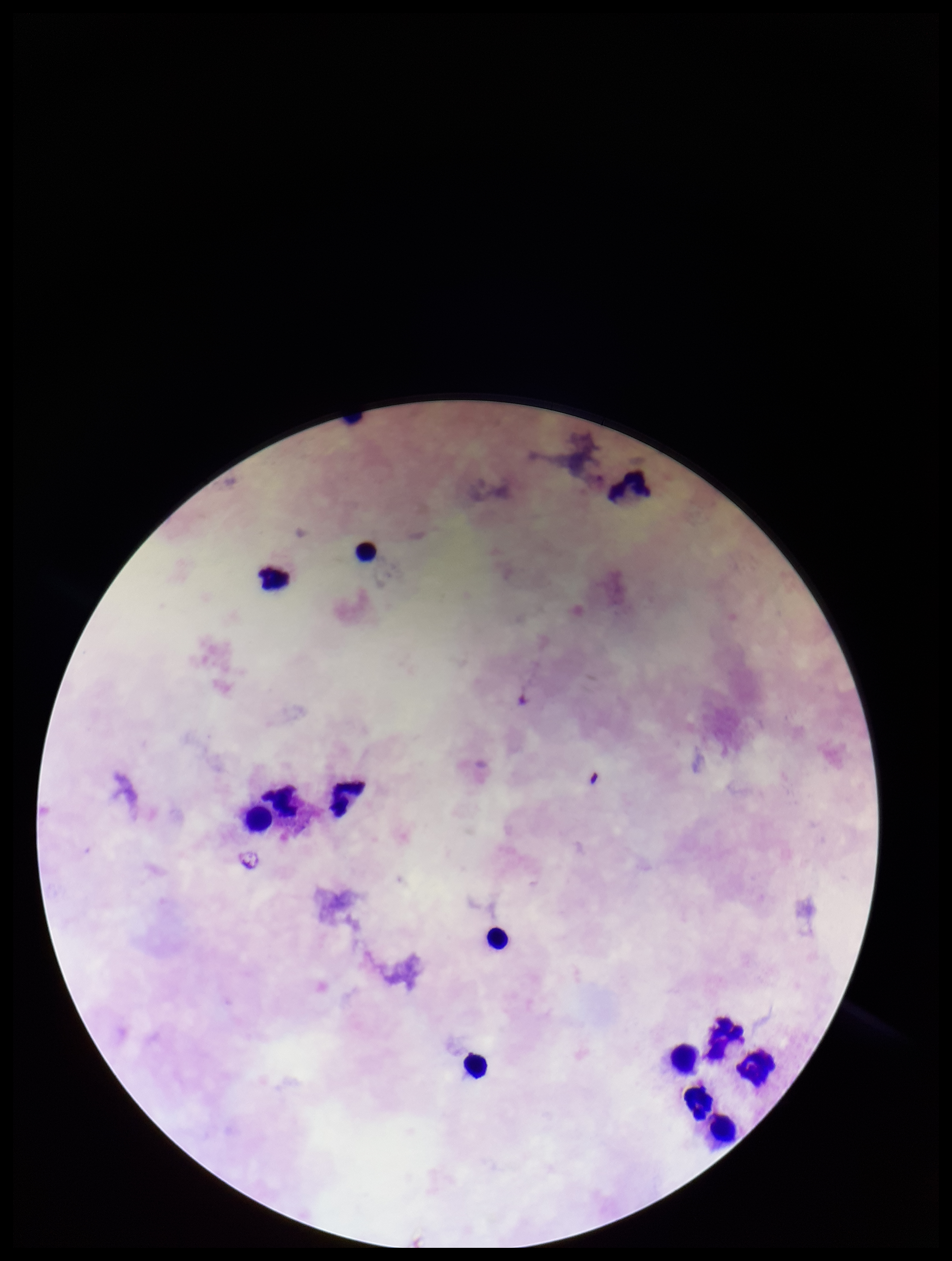 Photographed through the microscope eyepiece with a smartphone camera. Plasmodium parasites: none seen. Preparation: thick smear. Image is 952×1261 pixels. Leukocyte count: 13. Patient malaria status: negative. Parasite count: 0. One field from this slide. Stained with Giemsa.